Assess this cell for malaria.
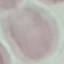
It is uninfected.

Giemsa stain. Thin blood film. Cell patch, automatically extracted from a larger field of view and resized to 64 × 64 pixels. Photographed with a smartphone camera at the microscope eyepiece.